Name the blood parasite species.
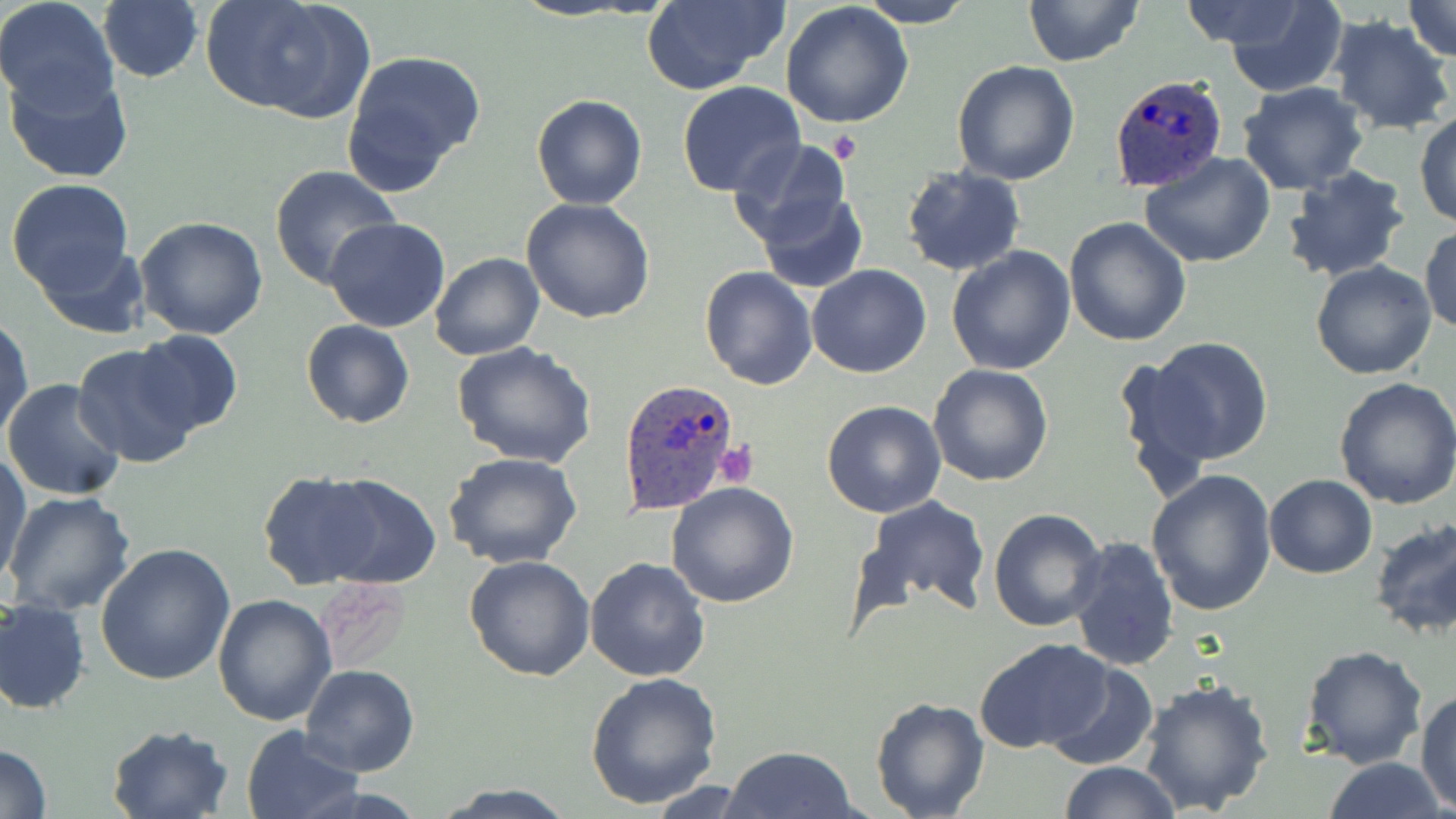

Plasmodium ovale.

Approximate bounding boxes as (x1,y1)-(x2,y2) corner pairs in pixels. Uninfected red blood cell locations: (97,0)-(204,84), (203,0)-(374,121), (640,0)-(788,93), (1023,0)-(1144,68), (1179,0)-(1324,54), (1222,0)-(1350,97), (1399,0)-(1456,62), (0,1)-(120,116), (858,1)-(974,27), (782,4)-(915,131), (1326,14)-(1454,135), (340,50)-(487,191), (951,60)-(1080,186), (4,66)-(134,185), (677,82)-(805,199), (1237,83)-(1369,195), (531,93)-(647,210), (1414,110)-(1456,228), (1254,112)-(1400,261), (728,138)-(856,254), (1141,152)-(1278,270), (1282,163)-(1412,282), (270,165)-(402,291), (900,166)-(1026,277), (5,178)-(134,299), (755,190)-(869,292), (522,198)-(655,322), (136,216)-(269,339), (323,218)-(452,333), (1063,218)-(1192,347), (1420,223)-(1455,335), (33,238)-(150,339), (945,246)-(1078,375), (429,252)-(544,360), (1311,261)-(1438,380), (699,265)-(817,389), (807,266)-(932,378), (1,312)-(33,448), (301,320)-(415,429), (133,329)-(244,436), (1139,337)-(1274,466), (451,341)-(598,468), (71,343)-(201,466), (928,364)-(1054,485), (1333,375)-(1456,510), (2,378)-(127,502), (822,400)-(947,517), (1,453)-(32,583), (444,453)-(584,571), (1145,467)-(1277,617), (258,470)-(387,590), (307,474)-(443,588), (1263,474)-(1377,579), (666,482)-(800,609), (4,489)-(135,614), (860,494)-(990,614), (989,507)-(1107,630), (1369,517)-(1456,640), (1066,536)-(1180,672), (98,544)-(238,686), (465,554)-(596,681), (585,557)-(712,682), (316,581)-(411,672), (213,593)-(338,725), (0,598)-(91,714), (973,638)-(1117,754), (1301,645)-(1429,769), (1046,661)-(1158,769), (300,666)-(419,776), (584,672)-(724,811), (1137,678)-(1277,816), (1416,689)-(1456,811), (869,696)-(990,819), (1383,710)-(1456,815), (106,724)-(232,819), (240,726)-(365,819), (0,744)-(52,819), (720,745)-(860,819), (1323,757)-(1448,819), (1058,760)-(1181,818), (647,780)-(758,816), (430,782)-(577,817). Plasmodium ovale-infected red blood cell locations: (1106,70)-(1230,193), (618,378)-(743,515). Platelet locations: (830,133)-(863,163), (715,441)-(758,488). May-Grünwald-Giemsa-stained preparation. One field of a larger specimen. Captured at 1000x magnification. Thin blood smear. Image is 1456×819 pixels. Light microscopy.